Classify this cell by malaria status.
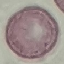
It is uninfected.

Acquired by smartphone through the microscope eyepiece. Cell patch, automatically extracted from a larger field of view and resized to 64 × 64 pixels. Giemsa stain. Thin blood smear.